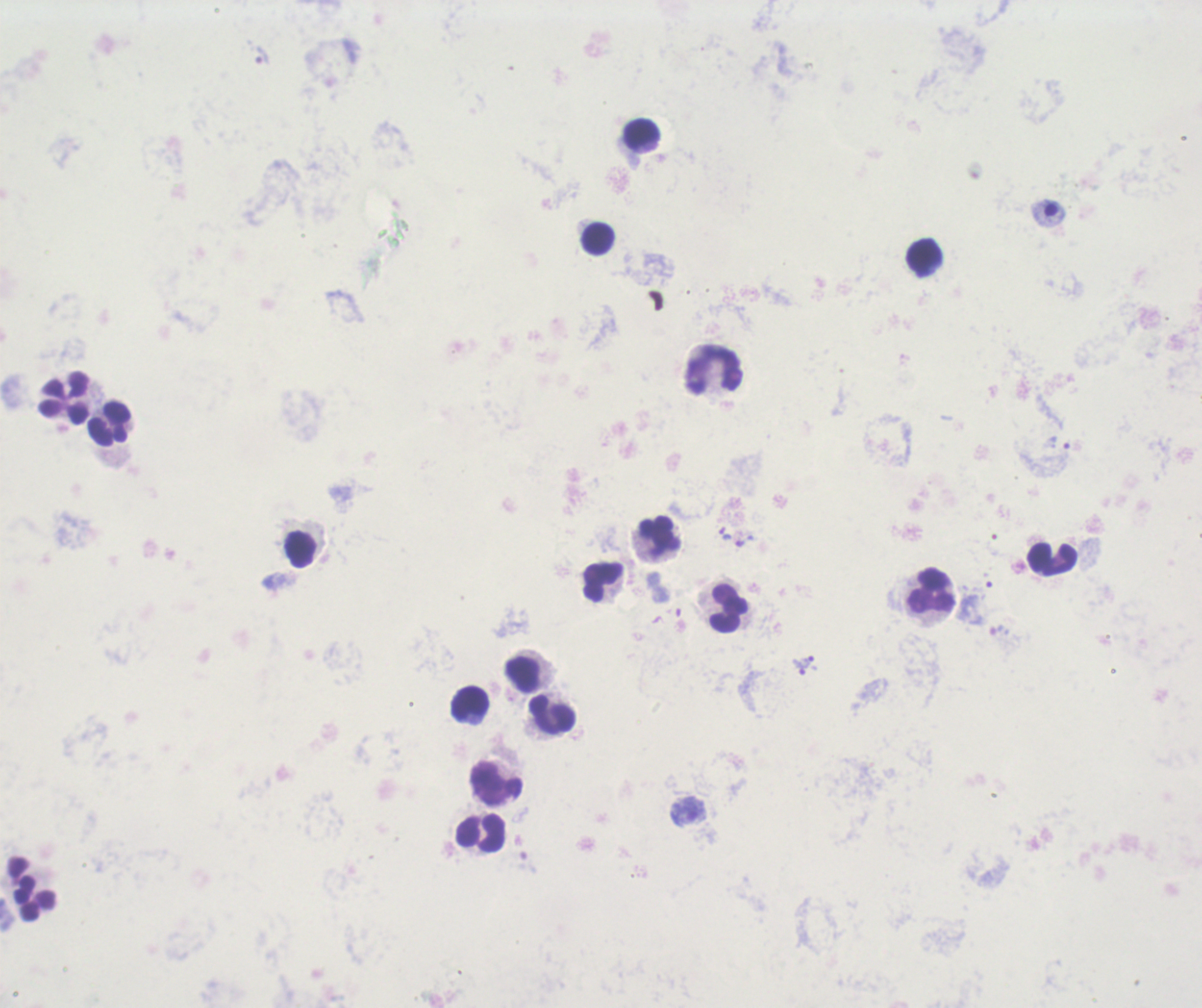

coordinate format = approximate centers as (x, y) in pixels
leukocyte locations = (642, 137), (596, 239), (923, 256), (715, 368), (61, 396), (110, 423), (661, 537), (302, 549), (1052, 558), (602, 580), (932, 591), (725, 608), (525, 674), (468, 705), (552, 715), (492, 781), (479, 832), (34, 886)
trophozoite locations = (1059, 443), (724, 534), (810, 660), (799, 666)
result = Plasmodium parasites detected
context = previously used in an actual diagnosis
background quality = poor
stain = Romanowsky
image size = 1202×1008 pixels
magnification = 100x
field of view = one from this slide
preparation = thick blood film